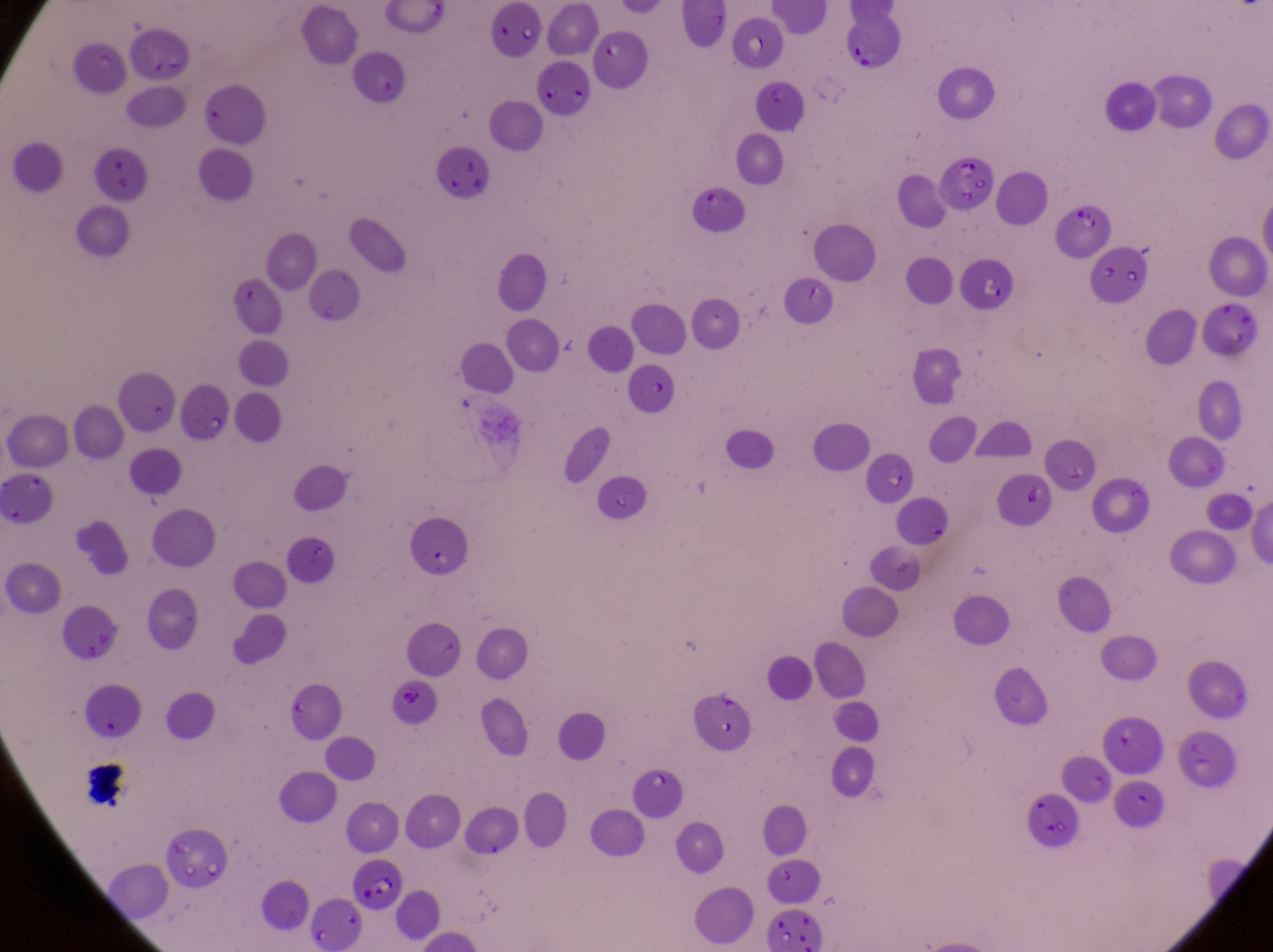
{
  "country": "Uganda",
  "field_of_view": "single",
  "parasitised_red_blood_cell_locations": "approximate bounding boxes as [left, top, right, bottom] in pixels: [934, 153, 1004, 216], [345, 859, 405, 919]",
  "image_size": "1273×952 pixels",
  "artifact_platelet_like_body_stain_precipitate_or_debris_locations": "approximate bounding boxes as [left, top, right, bottom] in pixels: [435, 147, 492, 210], [87, 150, 156, 205], [1061, 204, 1116, 257], [1006, 477, 1059, 525], [69, 756, 136, 811]",
  "capture": "smartphone photograph through the eyepiece of an Olympus CX-23 microscope",
  "preparation": "thin blood film",
  "magnification": "1000x"
}